Report the malaria status of this cell.
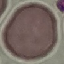

It is uninfected.

Giemsa stain. Thin blood smear. Photographed with a smartphone camera at the microscope eyepiece. Automatically extracted cell patch, resized to 64 × 64 pixels.